Comment on the morphology of the erythrocytes.
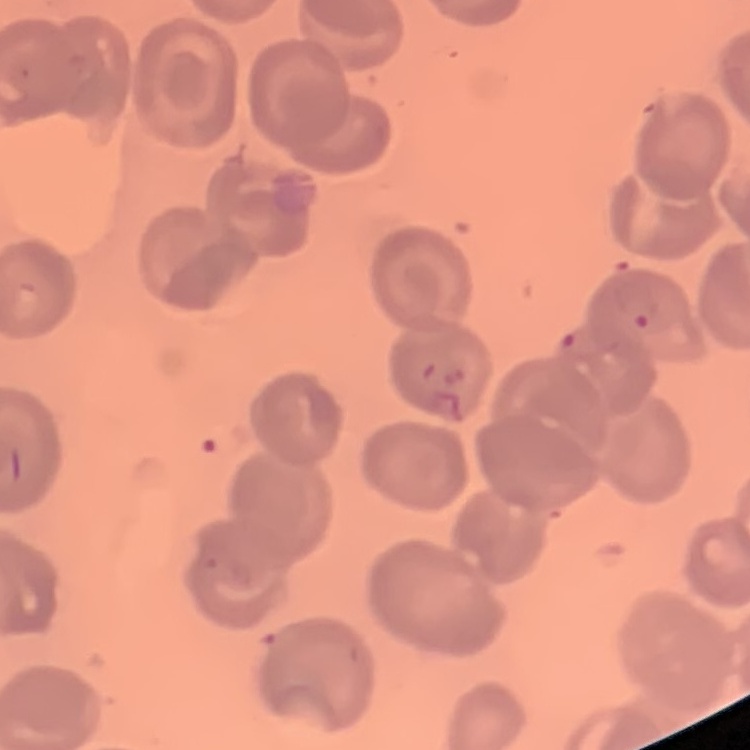
No rouleaux formation.

preparation = thin peripheral smear
stain = Field's or Giemsa
image type = square crop of a larger photomicrograph